Identify the parasite.
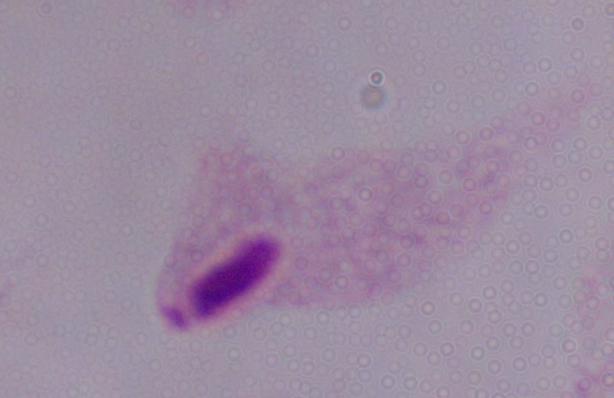

A trichomonad.

Summary:
  - Modality: photomicrograph
  - Magnification: 1000x